Classify this cell by malaria status.
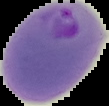

Parasitized.

{
  "image_type": "segmented cell region with the area outside set to black",
  "image_size": "109×106 pixels",
  "preparation": "thin blood smear"
}